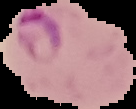

Image is 136×109 pixels. Result: Plasmodium parasites identified. Cell region segmented out of the field of view; the surrounding area is masked to black. From a thin blood film.